Assess this cell for malaria.
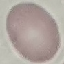
It is uninfected.

Automatically extracted cell patch, resized to 64 × 64 pixels. Giemsa-stained preparation. Thin blood smear. Acquired by smartphone through the microscope eyepiece.